Give the position of every Plasmodium parasite.
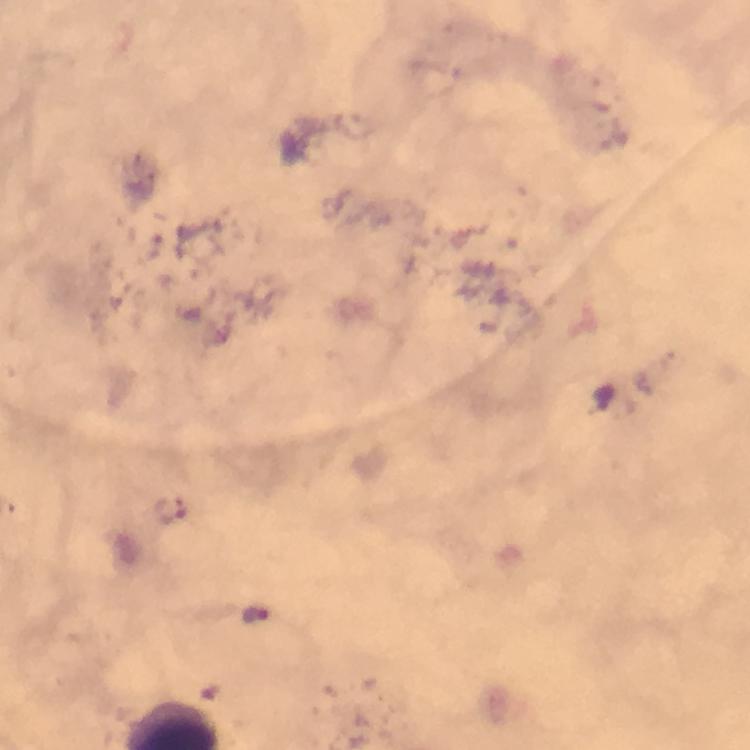
Approximate centers as (x, y) in pixels.
Plasmodium parasites: (169, 511), (256, 615).

Giemsa stain. Immersion oil was used. From a malaria diagnostic workup. Photographed with a smartphone mounted on the microscope. Image is 750×750 pixels. Thick blood film. Cropped region of a single field of view. At 100x magnification.